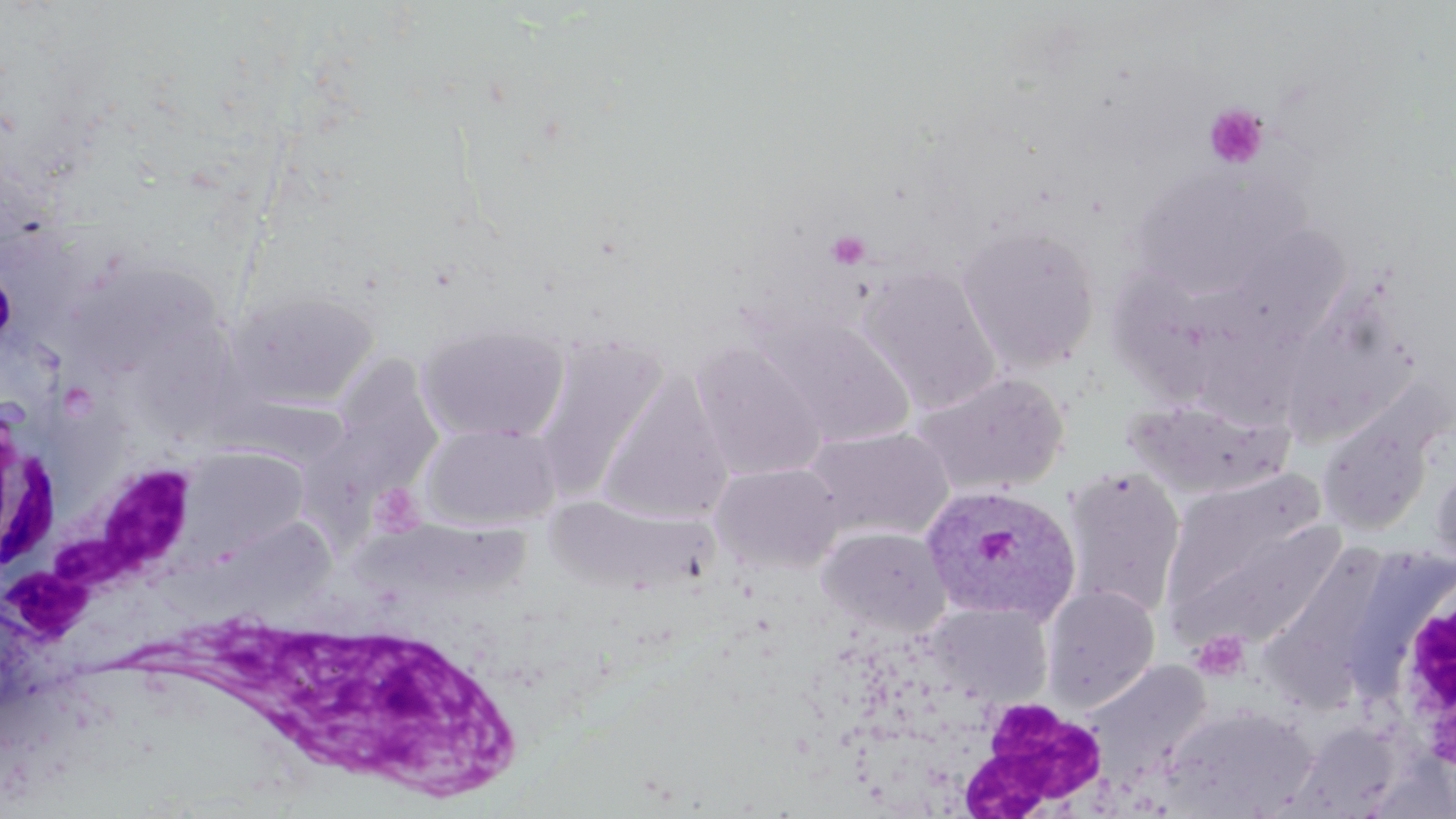

slide_level_diagnosis: Plasmodium ovale
field_of_view: one of a larger specimen
uninfected_red_blood_cell_locations: 'approximate bounding boxes as (x1, y1, x2, y2) in pixels: (1127, 165, 1292, 300), (956, 223, 1101, 372), (1196, 226, 1357, 414), (66, 256, 225, 378), (858, 265, 1003, 413), (226, 288, 380, 409), (762, 315, 916, 447), (417, 319, 571, 445), (532, 334, 668, 501), (690, 341, 828, 482), (327, 352, 448, 491), (912, 370, 1070, 497), (598, 372, 734, 524), (1123, 397, 1293, 499), (1316, 409, 1438, 538), (422, 423, 560, 529), (804, 426, 954, 542), (180, 446, 309, 559), (1429, 457, 1456, 579), (711, 462, 845, 574), (1062, 467, 1185, 618), (1156, 479, 1344, 654), (549, 496, 713, 597), (357, 525, 536, 604), (818, 526, 952, 636), (1262, 545, 1392, 707), (1041, 585, 1160, 710), (927, 602, 1054, 708), (1083, 660, 1215, 790), (1160, 703, 1317, 816)'
stain: May-Grünwald-Giemsa
modality: light microscopy
white_blood_cell_locations: 'approximate bounding boxes as (x1, y1, x2, y2) in pixels: (0, 458, 203, 666), (1384, 567, 1456, 775), (217, 602, 530, 810), (952, 698, 1110, 815)'
magnification: 1000x
preparation: thin blood film
plasmodium_ovale_infected_red_blood_cell_locations: 'approximate bounding boxes as (x1, y1, x2, y2) in pixels: (920, 483, 1081, 625)'
image_size: 1456×819 pixels
platelet_locations: 'approximate bounding boxes as (x1, y1, x2, y2) in pixels: (1204, 104, 1269, 169), (825, 229, 871, 270), (366, 479, 425, 537), (1191, 631, 1251, 681)'